Report the malaria status of this cell.
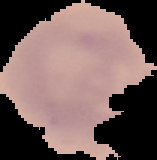
It is uninfected.

preparation = thin blood film
image size = 157×160 pixels
image type = segmented cell region on a black background